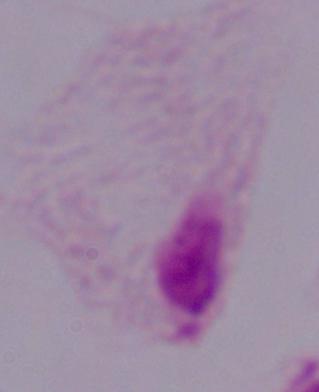
magnification: 1000x
modality: micrograph
identification: trichomonad